Report the malaria status of this cell.
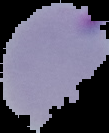
Parasitized.

{
  "image_type": "segmented cell region with the area outside set to black",
  "image_size": "109×133 pixels",
  "preparation": "thin blood smear"
}